Name the blood parasite species.
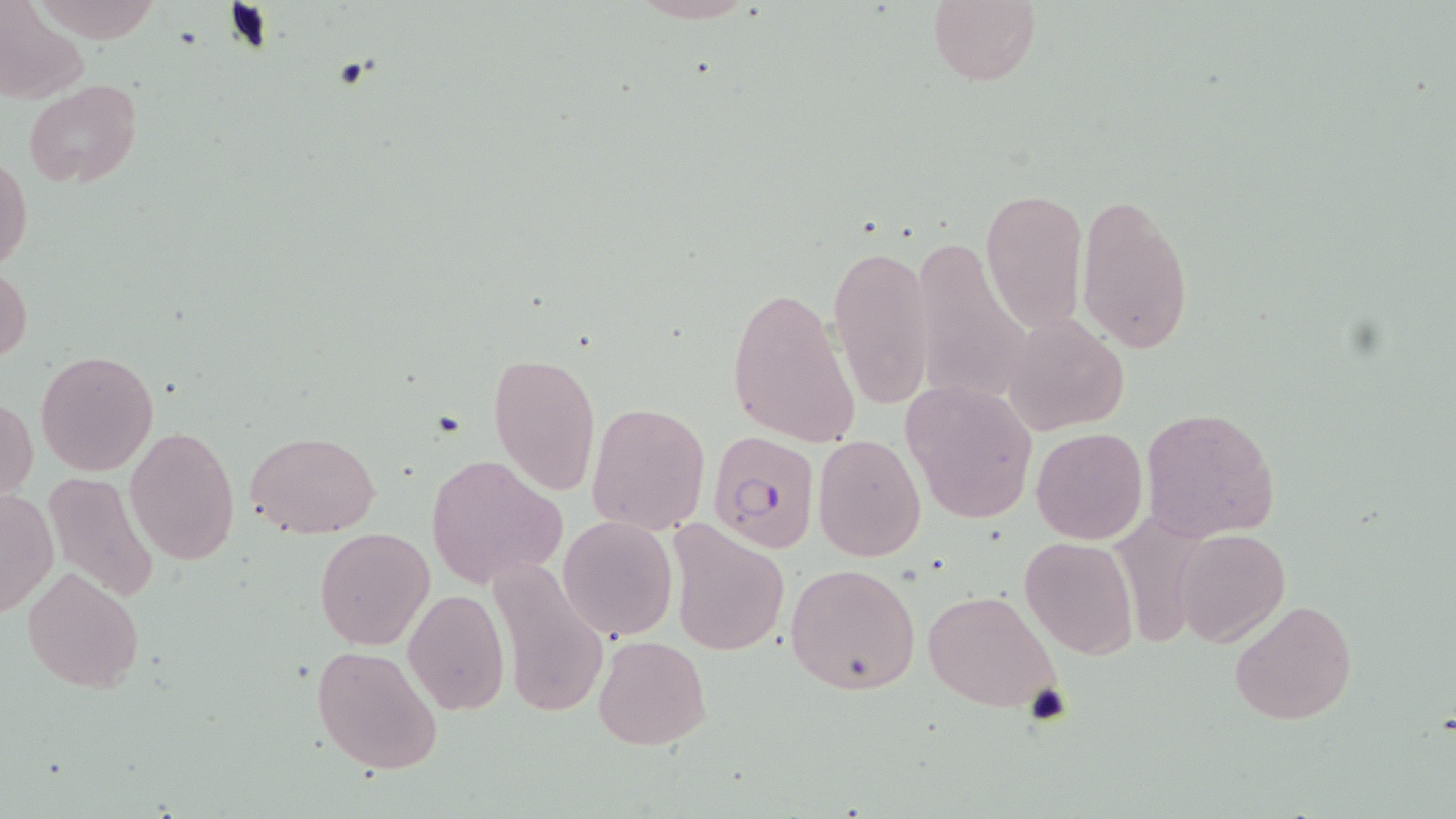

Plasmodium falciparum.

Summary:
  - Coordinate format: approximate bounding boxes as (x1,y1)-(x2,y2) corner pairs in pixels
  - Plasmodium falciparum-infected red blood cell locations: (708,434)-(820,554)
  - Uninfected red blood cell locations: (626,0)-(761,25), (928,0)-(1040,87), (2,5)-(86,102), (23,80)-(142,187), (0,156)-(32,273), (979,187)-(1087,331), (1076,193)-(1195,355), (909,239)-(1034,411), (828,243)-(935,409), (1,266)-(31,362), (725,283)-(861,449), (1003,315)-(1129,434), (35,350)-(159,476), (487,350)-(602,495), (899,379)-(1040,525), (1,399)-(37,503), (587,402)-(711,534), (1141,406)-(1282,541), (125,426)-(241,567), (1030,426)-(1148,545), (246,431)-(380,537), (813,434)-(926,561), (426,453)-(566,589), (43,472)-(162,603), (0,489)-(55,617), (557,516)-(676,641), (667,518)-(791,658), (314,527)-(435,649), (1171,529)-(1289,647), (1019,536)-(1139,658), (485,551)-(609,724), (785,562)-(921,695), (21,565)-(145,695), (404,587)-(510,716), (922,588)-(1064,714), (1228,598)-(1358,726), (592,635)-(710,750), (311,642)-(442,776)
  - Modality: light microscopy
  - Preparation: thin blood smear
  - Field of view: one of a larger specimen
  - Image size: 1456×819 pixels
  - Stain: May-Grünwald-Giemsa
  - Magnification: 1000x